Classify this cell by malaria status.
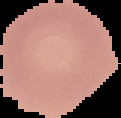
Uninfected.

Summary:
  - Preparation: thin blood smear
  - Image type: segmented cell region on a black background
  - Image size: 121×118 pixels